Classify this cell by malaria status.
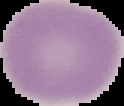
Uninfected.

From a thin blood film. Segmented cell region on a black background. Image is 124×106 pixels.